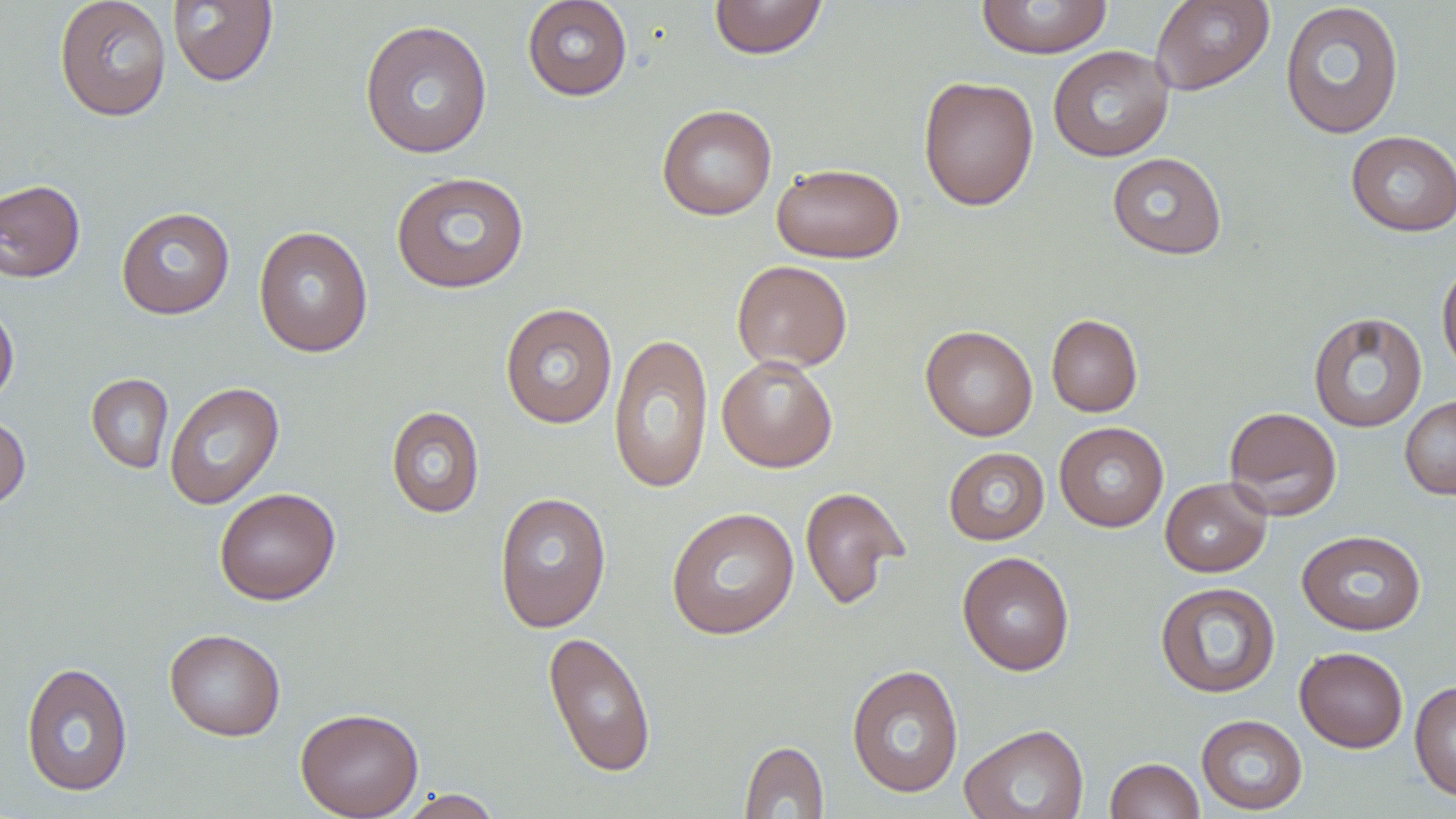

Approximate bounding boxes as [x1, y1, x2, y2] in pixels. Uninfected red blood cell locations: [54, 0, 172, 121], [521, 0, 633, 101], [708, 0, 828, 59], [975, 0, 1113, 59], [1150, 0, 1275, 95], [167, 1, 278, 87], [1279, 2, 1405, 139], [359, 19, 493, 159], [1047, 45, 1174, 162], [917, 76, 1039, 211], [656, 104, 778, 221], [1345, 130, 1456, 237], [1107, 152, 1227, 260], [771, 163, 904, 263], [390, 170, 529, 294], [0, 179, 85, 282], [116, 206, 235, 319], [253, 226, 374, 357], [1437, 259, 1456, 381], [731, 260, 853, 372], [0, 300, 19, 409], [500, 303, 618, 428], [1308, 312, 1428, 432], [1046, 314, 1143, 417], [920, 325, 1038, 441], [608, 331, 713, 494], [716, 355, 838, 472], [86, 373, 174, 473], [164, 381, 285, 509], [1400, 396, 1456, 499], [386, 406, 485, 518], [1223, 406, 1342, 521], [0, 413, 31, 509], [1054, 421, 1169, 532], [943, 447, 1049, 545], [1160, 477, 1271, 577], [800, 486, 910, 610], [214, 487, 341, 605], [494, 491, 612, 633], [665, 506, 800, 640], [1296, 530, 1427, 636], [956, 551, 1075, 676], [1154, 580, 1280, 698], [164, 628, 286, 741], [543, 631, 657, 778], [1295, 646, 1408, 753], [21, 661, 133, 798], [846, 664, 964, 798], [1409, 679, 1456, 802], [295, 707, 424, 819], [1196, 714, 1307, 815], [960, 723, 1090, 819], [739, 741, 829, 818], [1105, 757, 1205, 818], [397, 788, 503, 819]. Slide-level diagnosis: no evidence of blood parasites. Thin blood film. Captured at 1000x magnification. May-Grünwald-Giemsa-stained preparation. Optical microscopy. One field of a larger specimen. Image is 1456×819 pixels.